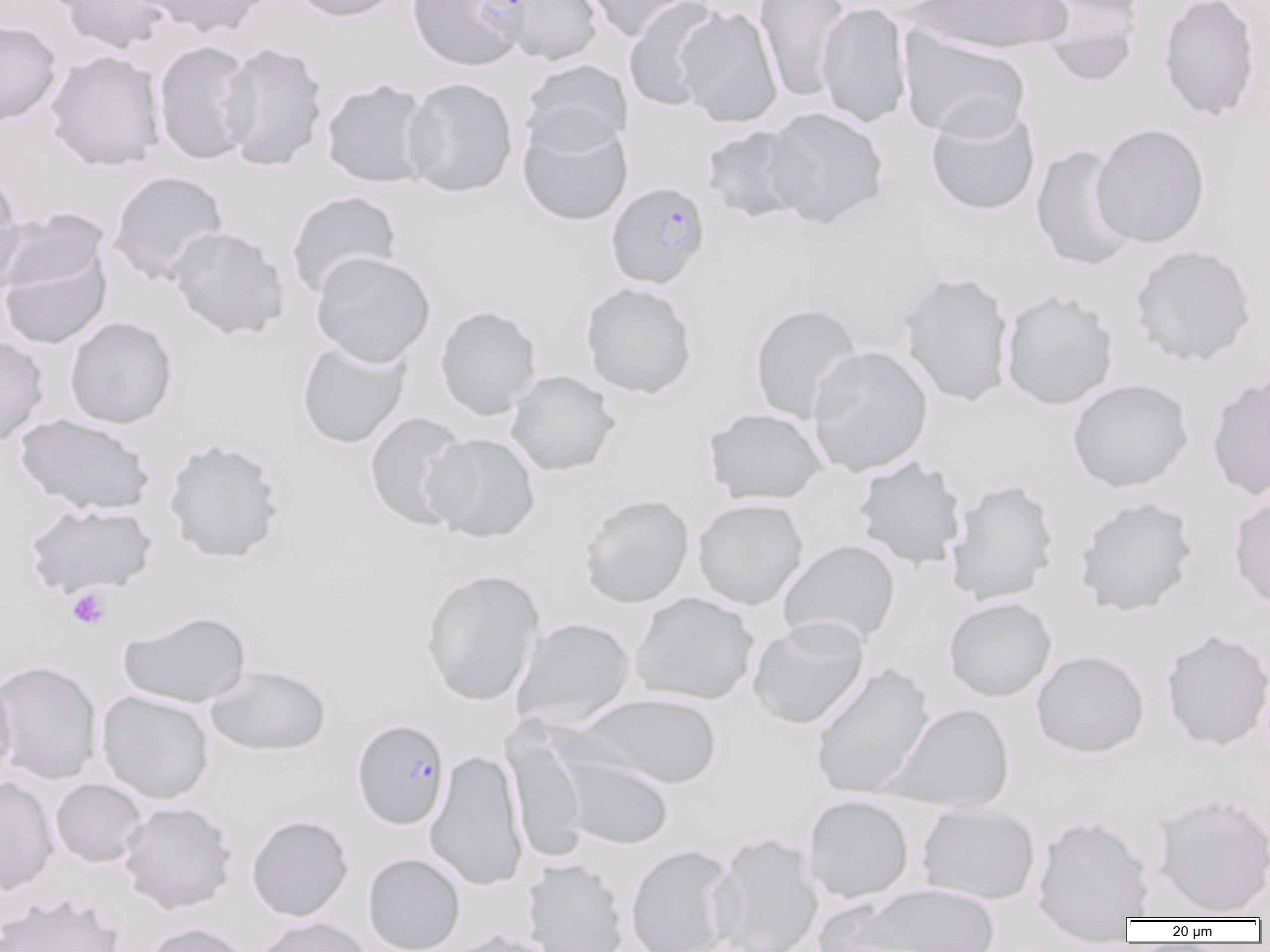

Approximate bounding boxes as named x1/y1/x2/y2 corners in pixels. Uninfected red blood cell locations: (x1=55, y1=0, x2=174, y2=55), (x1=139, y1=0, x2=274, y2=38), (x1=288, y1=0, x2=407, y2=23), (x1=493, y1=0, x2=605, y2=66), (x1=579, y1=0, x2=698, y2=41), (x1=623, y1=0, x2=725, y2=111), (x1=754, y1=0, x2=852, y2=101), (x1=910, y1=0, x2=1074, y2=53), (x1=1158, y1=0, x2=1261, y2=121), (x1=816, y1=2, x2=913, y2=128), (x1=1034, y1=2, x2=1143, y2=86), (x1=675, y1=6, x2=783, y2=128), (x1=0, y1=19, x2=63, y2=127), (x1=898, y1=27, x2=1032, y2=141), (x1=152, y1=40, x2=256, y2=164), (x1=218, y1=42, x2=328, y2=171), (x1=45, y1=50, x2=165, y2=171), (x1=520, y1=60, x2=633, y2=156), (x1=401, y1=77, x2=518, y2=197), (x1=321, y1=79, x2=434, y2=188), (x1=925, y1=105, x2=1040, y2=215), (x1=763, y1=107, x2=888, y2=228), (x1=517, y1=117, x2=633, y2=227), (x1=1090, y1=122, x2=1210, y2=247), (x1=701, y1=125, x2=809, y2=224), (x1=1030, y1=144, x2=1138, y2=271), (x1=0, y1=169, x2=25, y2=293), (x1=107, y1=170, x2=228, y2=286), (x1=286, y1=191, x2=402, y2=299), (x1=1, y1=208, x2=110, y2=299), (x1=167, y1=226, x2=289, y2=340), (x1=0, y1=243, x2=113, y2=351), (x1=1129, y1=244, x2=1257, y2=366), (x1=311, y1=251, x2=435, y2=368), (x1=899, y1=271, x2=1015, y2=406), (x1=580, y1=283, x2=697, y2=398), (x1=1000, y1=289, x2=1118, y2=410), (x1=749, y1=304, x2=863, y2=423), (x1=435, y1=305, x2=541, y2=421), (x1=64, y1=316, x2=177, y2=429), (x1=0, y1=334, x2=49, y2=446), (x1=296, y1=339, x2=411, y2=449), (x1=807, y1=345, x2=933, y2=477), (x1=1206, y1=369, x2=1270, y2=502), (x1=505, y1=370, x2=620, y2=476), (x1=1067, y1=379, x2=1193, y2=492), (x1=704, y1=408, x2=828, y2=504), (x1=364, y1=412, x2=472, y2=531), (x1=14, y1=413, x2=156, y2=516), (x1=423, y1=433, x2=541, y2=542), (x1=163, y1=438, x2=284, y2=563), (x1=852, y1=457, x2=966, y2=570), (x1=945, y1=479, x2=1060, y2=605), (x1=1228, y1=493, x2=1270, y2=609), (x1=579, y1=494, x2=694, y2=608), (x1=1073, y1=496, x2=1198, y2=617), (x1=692, y1=498, x2=808, y2=610), (x1=24, y1=503, x2=157, y2=598), (x1=778, y1=539, x2=901, y2=647), (x1=420, y1=568, x2=545, y2=706), (x1=630, y1=592, x2=758, y2=705), (x1=944, y1=598, x2=1056, y2=701), (x1=118, y1=610, x2=251, y2=708), (x1=747, y1=616, x2=869, y2=730), (x1=512, y1=617, x2=635, y2=729), (x1=1160, y1=629, x2=1270, y2=751), (x1=1031, y1=650, x2=1149, y2=758), (x1=0, y1=660, x2=103, y2=784), (x1=810, y1=662, x2=934, y2=800), (x1=206, y1=665, x2=331, y2=757), (x1=0, y1=672, x2=17, y2=787), (x1=96, y1=691, x2=214, y2=804), (x1=569, y1=693, x2=722, y2=790), (x1=885, y1=703, x2=1015, y2=813), (x1=505, y1=727, x2=589, y2=863), (x1=425, y1=750, x2=528, y2=891), (x1=557, y1=753, x2=675, y2=850), (x1=0, y1=777, x2=58, y2=895), (x1=50, y1=779, x2=148, y2=867), (x1=1151, y1=793, x2=1270, y2=917), (x1=803, y1=795, x2=914, y2=903), (x1=118, y1=802, x2=237, y2=913), (x1=917, y1=802, x2=1040, y2=904), (x1=246, y1=815, x2=353, y2=922), (x1=1032, y1=815, x2=1154, y2=937), (x1=708, y1=833, x2=822, y2=952), (x1=625, y1=845, x2=736, y2=952), (x1=362, y1=853, x2=465, y2=952), (x1=522, y1=858, x2=629, y2=952), (x1=845, y1=884, x2=1001, y2=952), (x1=0, y1=893, x2=125, y2=952), (x1=252, y1=917, x2=375, y2=952), (x1=141, y1=922, x2=252, y2=952), (x1=438, y1=929, x2=561, y2=952). Platelet locations: (x1=66, y1=587, x2=111, y2=630). Plasmodium falciparum-infected red blood cell locations: (x1=406, y1=0, x2=530, y2=70), (x1=606, y1=181, x2=711, y2=289), (x1=351, y1=718, x2=450, y2=829). Slide-level diagnosis: Plasmodium falciparum. Optical microscopy. Thin blood film. One field of a larger specimen. Image is 1270×952 pixels. Captured at 1000x magnification.